Outline every Plasmodium parasite.
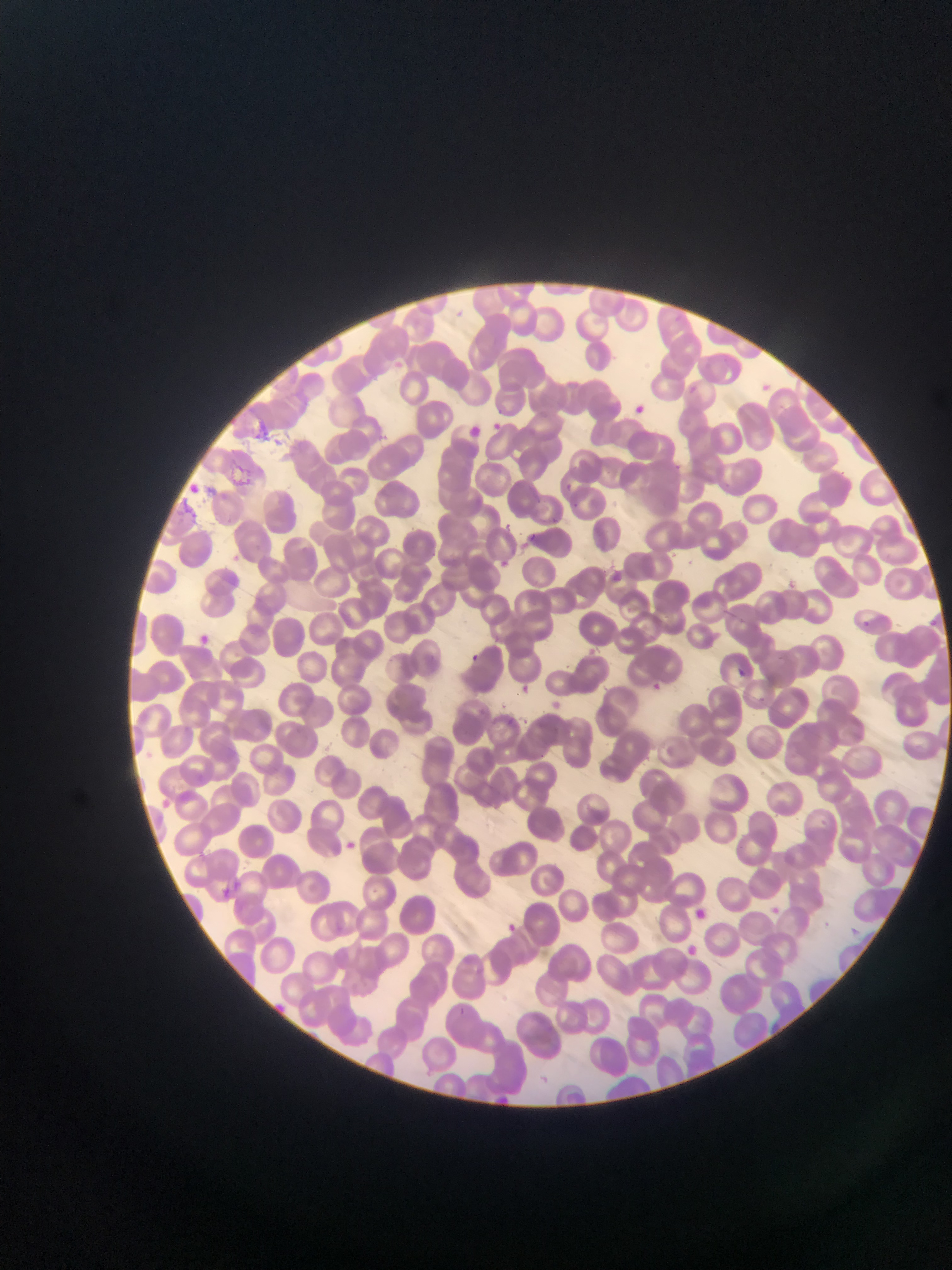

Approximate bounding boxes as (left, top, right, bottom) in pixels.
Plasmodium parasites: (625, 400, 652, 422), (481, 419, 509, 440), (489, 420, 507, 435), (463, 424, 485, 443), (190, 630, 214, 650), (464, 649, 484, 668), (734, 665, 749, 680), (648, 680, 666, 692), (516, 682, 533, 697), (340, 836, 361, 854), (767, 905, 782, 918), (502, 920, 520, 936).

Photographed through a microscope with a mobile-phone camera. Image is 952×1270 pixels. Sample from Ghana. One field of view. Thin blood film.